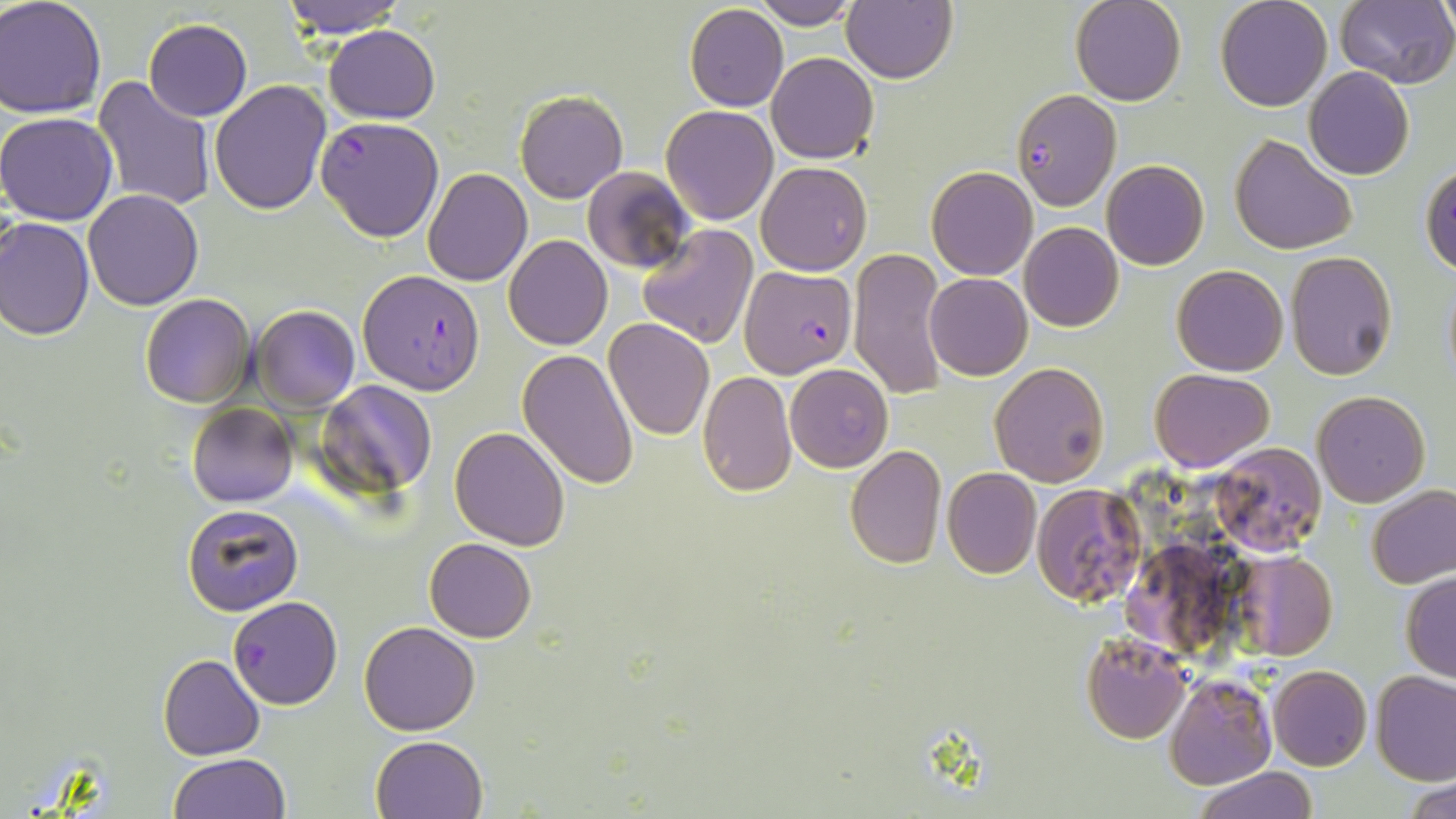

{
  "slide_level_diagnosis": "Plasmodium falciparum",
  "modality": "light microscopy",
  "plasmodium_falciparum_infected_red_blood_cell_locations": "approximate bounding boxes as named x1/y1/x2/y2 corners in pixels: (x1=1009, y1=89, x2=1121, y2=210), (x1=316, y1=116, x2=444, y2=242), (x1=739, y1=266, x2=857, y2=377), (x1=357, y1=269, x2=486, y2=393), (x1=229, y1=595, x2=342, y2=709)",
  "stain": "May-Grünwald-Giemsa",
  "field_of_view": "single",
  "uninfected_red_blood_cell_locations": "approximate bounding boxes as named x1/y1/x2/y2 corners in pixels: (x1=0, y1=0, x2=106, y2=119), (x1=279, y1=0, x2=406, y2=38), (x1=843, y1=0, x2=957, y2=83), (x1=1070, y1=0, x2=1185, y2=106), (x1=1215, y1=0, x2=1332, y2=112), (x1=751, y1=1, x2=861, y2=30), (x1=1334, y1=1, x2=1456, y2=88), (x1=684, y1=4, x2=788, y2=111), (x1=143, y1=19, x2=251, y2=122), (x1=323, y1=25, x2=440, y2=123), (x1=767, y1=52, x2=879, y2=164), (x1=1303, y1=67, x2=1415, y2=180), (x1=93, y1=75, x2=217, y2=213), (x1=208, y1=79, x2=332, y2=215), (x1=515, y1=91, x2=628, y2=204), (x1=661, y1=105, x2=778, y2=224), (x1=654, y1=109, x2=768, y2=347), (x1=0, y1=112, x2=120, y2=225), (x1=1229, y1=133, x2=1356, y2=255), (x1=1101, y1=160, x2=1209, y2=270), (x1=757, y1=162, x2=871, y2=275), (x1=1421, y1=163, x2=1456, y2=275), (x1=583, y1=165, x2=697, y2=275), (x1=423, y1=168, x2=532, y2=286), (x1=926, y1=168, x2=1037, y2=280), (x1=82, y1=189, x2=205, y2=310), (x1=0, y1=216, x2=95, y2=339), (x1=1019, y1=223, x2=1123, y2=332), (x1=637, y1=225, x2=759, y2=350), (x1=504, y1=234, x2=612, y2=351), (x1=849, y1=247, x2=950, y2=404), (x1=1286, y1=251, x2=1397, y2=380), (x1=1172, y1=264, x2=1288, y2=376), (x1=1441, y1=270, x2=1456, y2=392), (x1=925, y1=273, x2=1032, y2=380), (x1=139, y1=294, x2=255, y2=408), (x1=252, y1=305, x2=359, y2=412), (x1=605, y1=317, x2=714, y2=439), (x1=516, y1=348, x2=638, y2=490), (x1=990, y1=361, x2=1109, y2=485), (x1=785, y1=363, x2=893, y2=473), (x1=1150, y1=368, x2=1273, y2=470), (x1=698, y1=371, x2=799, y2=497), (x1=315, y1=380, x2=439, y2=498), (x1=1312, y1=391, x2=1430, y2=508), (x1=187, y1=402, x2=297, y2=507), (x1=449, y1=425, x2=571, y2=549), (x1=1209, y1=443, x2=1324, y2=555), (x1=845, y1=445, x2=947, y2=569), (x1=942, y1=468, x2=1041, y2=579), (x1=1031, y1=482, x2=1148, y2=607), (x1=1366, y1=484, x2=1456, y2=589), (x1=183, y1=502, x2=304, y2=616), (x1=424, y1=537, x2=536, y2=642), (x1=1115, y1=542, x2=1224, y2=667), (x1=1230, y1=552, x2=1338, y2=660), (x1=1401, y1=573, x2=1456, y2=683), (x1=359, y1=621, x2=480, y2=735), (x1=1081, y1=633, x2=1190, y2=744), (x1=158, y1=654, x2=265, y2=759), (x1=1268, y1=664, x2=1371, y2=771), (x1=1372, y1=670, x2=1456, y2=784), (x1=1163, y1=674, x2=1277, y2=790), (x1=372, y1=735, x2=488, y2=819), (x1=168, y1=753, x2=291, y2=818), (x1=1194, y1=767, x2=1317, y2=819), (x1=1404, y1=779, x2=1456, y2=819)",
  "magnification": "1000x",
  "preparation": "thin blood film",
  "image_size": "1456×819 pixels"
}